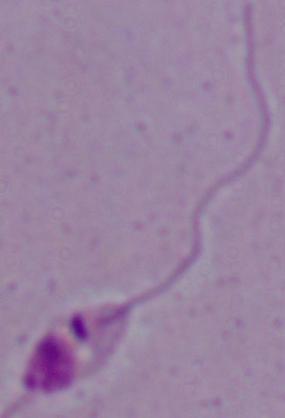
Summary:
  - Magnification: 1000x
  - Modality: micrograph
  - Identification: Leishmania